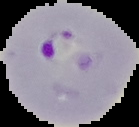

{
  "preparation": "thin blood film",
  "result": "malaria parasites identified",
  "image_size": "139×127 pixels",
  "image_type": "segmented cell region on a black background"
}